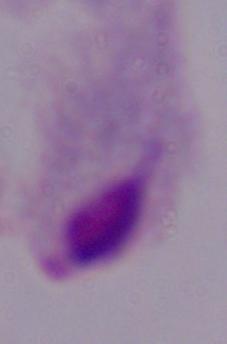
magnification = 1000x
identification = trichomonad
modality = photomicrograph